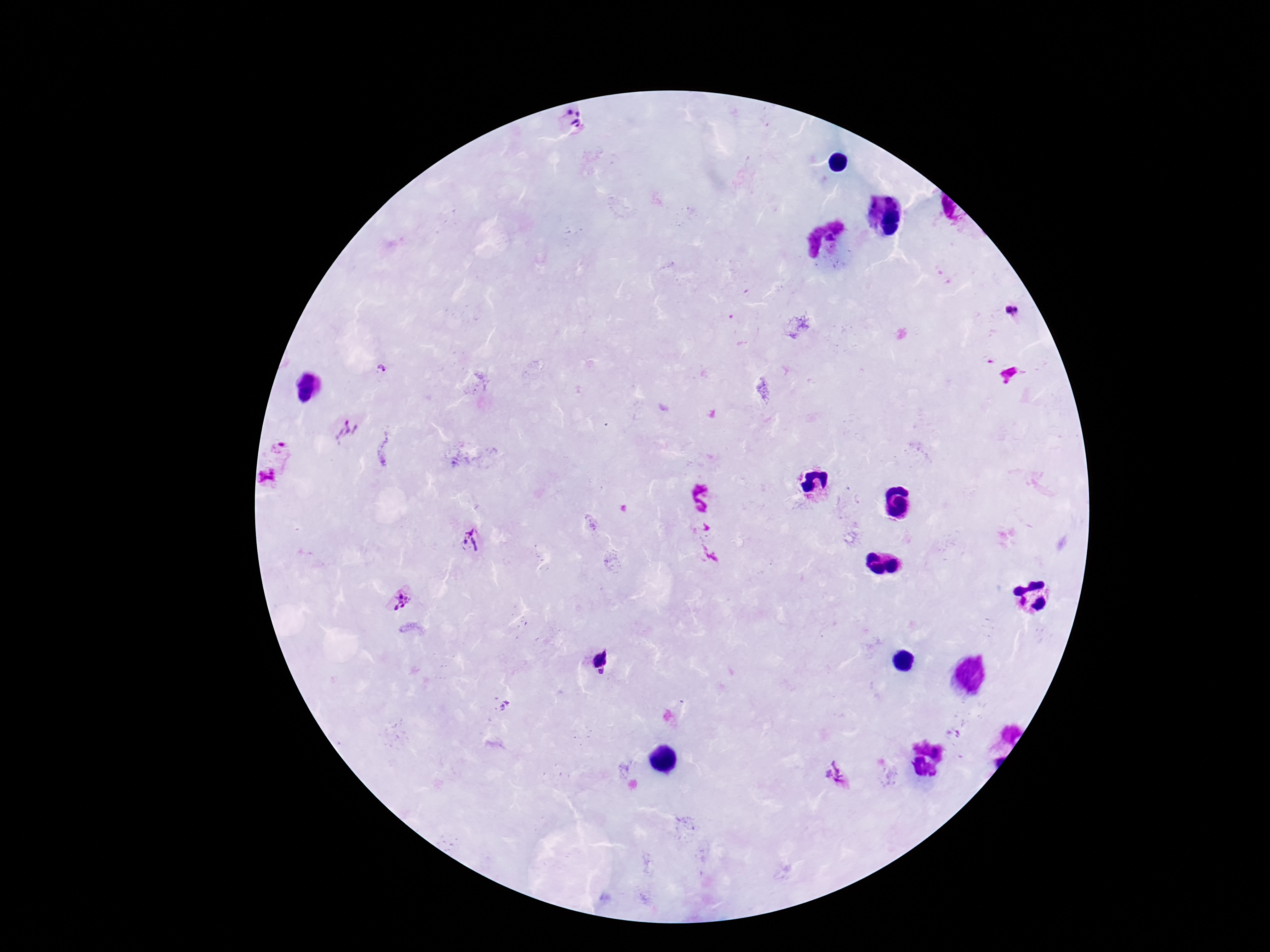
{
  "plasmodium_parasite_locations": "approximate centers as (x, y) in pixels: (575, 120), (1010, 311), (381, 369), (347, 431), (282, 444), (268, 476), (471, 538), (399, 599), (600, 655), (603, 672), (837, 774)",
  "stain": "Giemsa",
  "magnification": "100x",
  "field_of_view": "one from this slide",
  "capture": "smartphone camera through the microscope eyepiece",
  "preparation": "thick blood film",
  "patient_malaria_status": "positive",
  "image_size": "1270×952 pixels"
}